State which parasite is depicted.
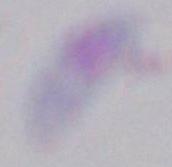

Toxoplasma gondii.

Summary:
  - Modality: micrograph
  - Magnification: 1000x